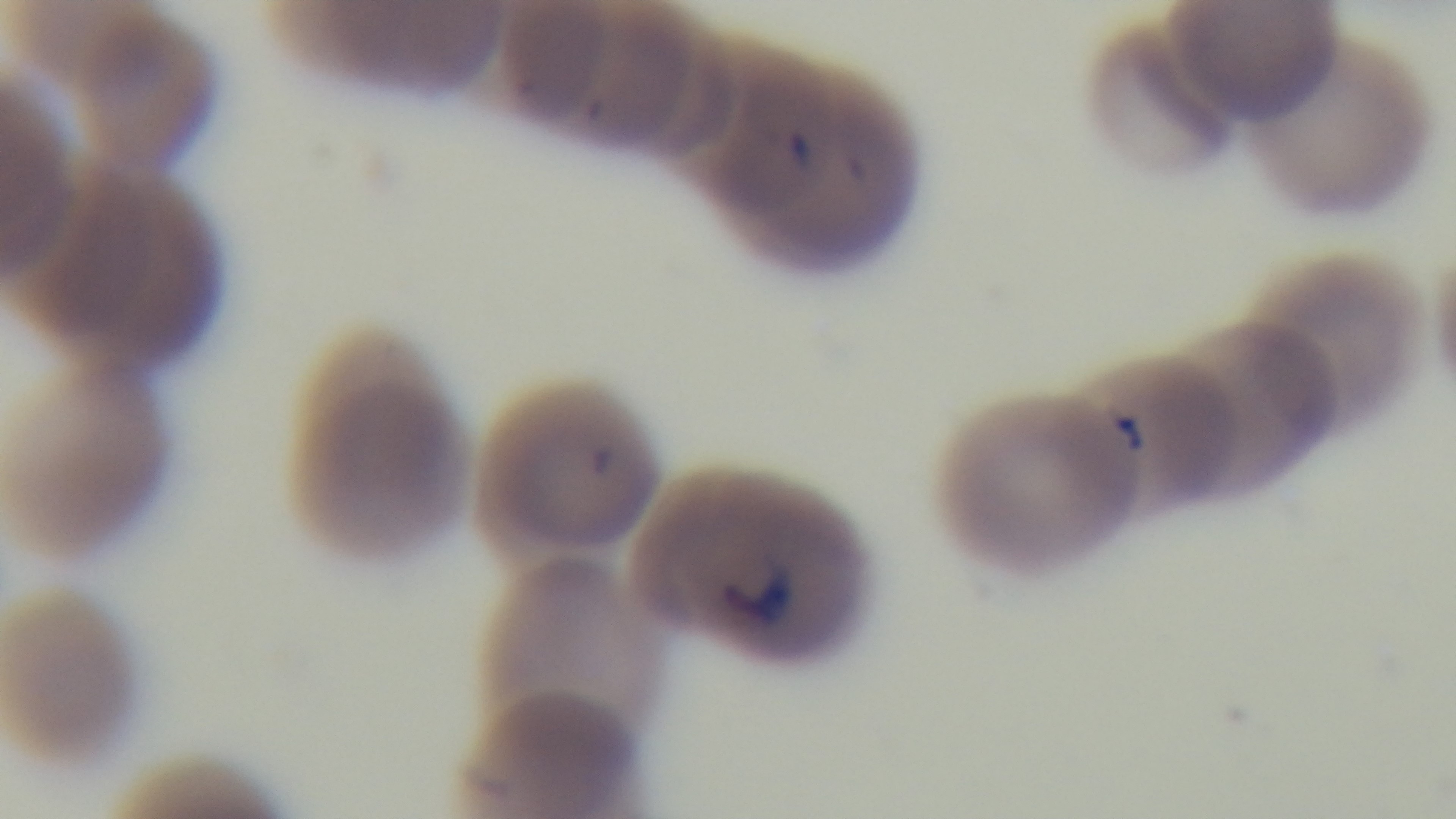

Summary:
  - Stain: Giemsa
  - Field of view: one from the slide
  - Preparation: thin
  - Malaria status: infected
  - Objective: 100x oil immersion
  - Capture: mounted 4K digital camera
  - Modality: light microscopy